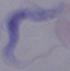
{
  "modality": "photomicrograph",
  "identification": "trypanosome",
  "magnification": "1000x"
}